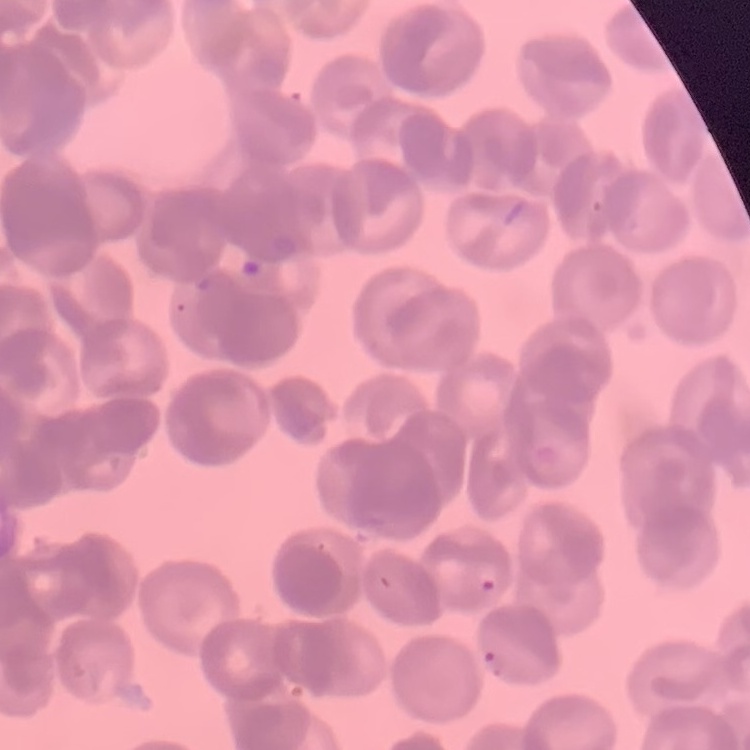

red blood cell morphology = rouleaux formation
stain = Field's or Giemsa
image type = square crop of a larger photomicrograph
preparation = thin blood film